Report the malaria status of this cell.
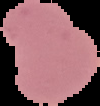
It is parasitized.

Summary:
  - Preparation: thin blood smear
  - Image size: 100×106 pixels
  - Image type: segmented cell region on a black background